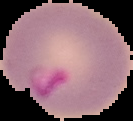
Summary:
  - Image type: cell region segmented out of the field of view; surrounding area masked to black
  - Image size: 133×121 pixels
  - Malaria status: parasitized
  - Preparation: thin blood film